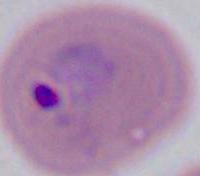 Captured at either 400x or 1000x magnification. Micrograph. A Plasmodium parasite is seen.